Give the extent of all Plasmodium falciparum-infected red blood cells.
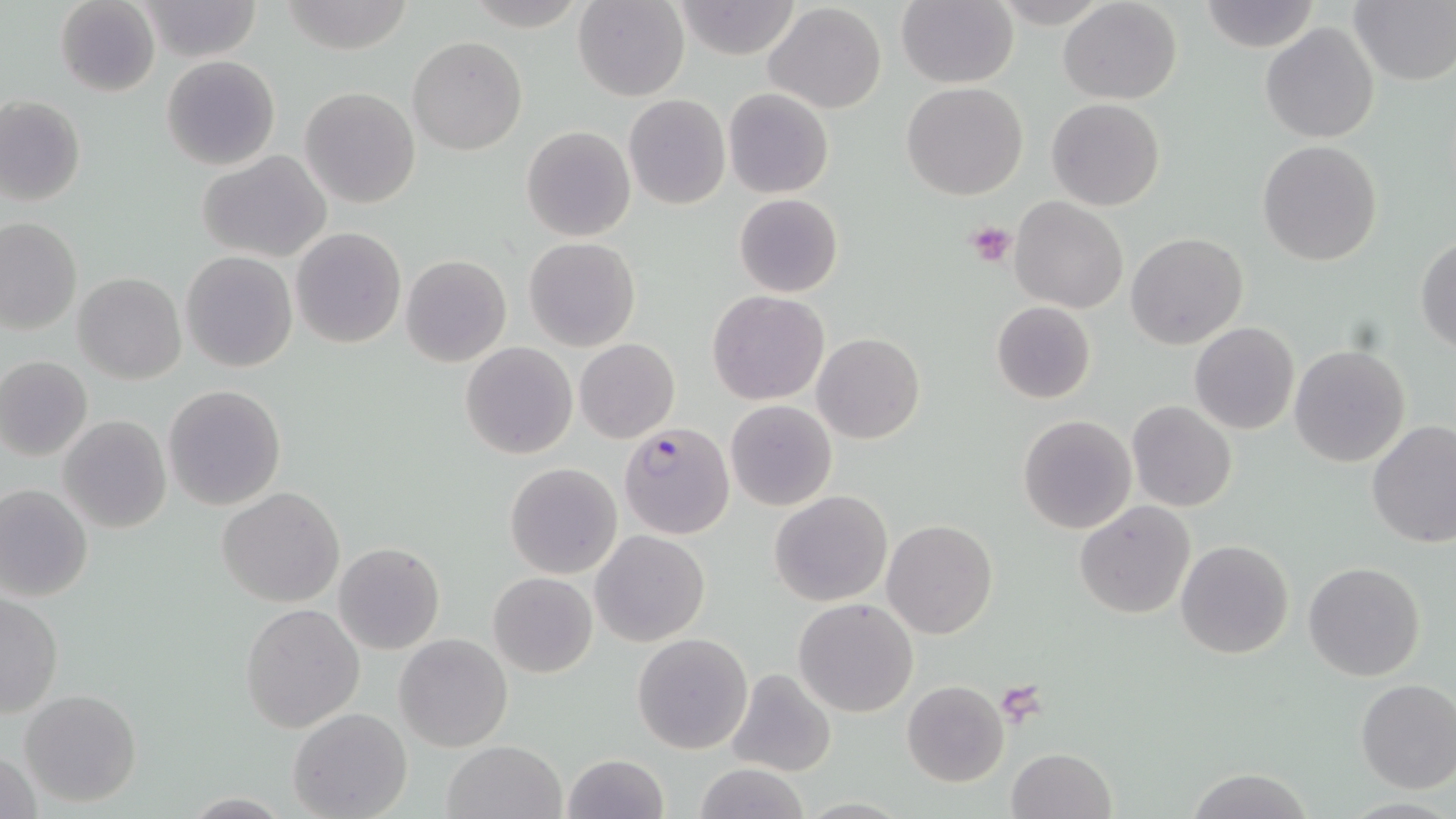

Approximate bounding boxes as (x1,y1)-(x2,y2) corner pairs in pixels.
Plasmodium falciparum-infected red blood cells: (618,421)-(732,540).

Platelet locations: (965,220)-(1018,267), (996,681)-(1048,721). Uninfected red blood cell locations: (137,0)-(264,61), (573,0)-(688,101), (897,0)-(1018,88), (1058,0)-(1184,105), (1198,0)-(1319,52), (56,1)-(160,97), (672,1)-(804,61), (1350,2)-(1455,85), (762,3)-(887,114), (1260,23)-(1380,145), (408,36)-(527,155), (161,55)-(281,171), (902,82)-(1030,201), (299,86)-(420,209), (723,88)-(834,198), (623,95)-(730,209), (0,96)-(86,206), (1046,97)-(1165,211), (520,126)-(636,242), (1257,141)-(1383,266), (197,150)-(332,261), (734,193)-(843,297), (1010,198)-(1128,314), (1,218)-(81,334), (290,227)-(407,348), (1126,233)-(1249,350), (1416,235)-(1456,353), (525,237)-(641,353), (180,251)-(298,372), (400,255)-(512,368), (74,273)-(186,386), (707,290)-(830,406), (991,300)-(1096,404), (1190,323)-(1299,435), (812,332)-(925,443), (574,338)-(679,442), (461,341)-(578,459), (1289,345)-(1411,469), (0,356)-(93,461), (163,384)-(287,511), (724,399)-(838,511), (1126,400)-(1238,512), (1017,414)-(1138,534), (59,415)-(172,533), (1366,422)-(1456,552), (505,462)-(622,578), (0,483)-(94,603), (217,486)-(346,607), (768,489)-(893,606), (1074,500)-(1196,620), (882,519)-(999,639), (590,529)-(711,647), (1174,538)-(1294,659), (335,542)-(444,654), (1303,562)-(1427,682), (488,572)-(597,677), (0,591)-(63,718), (794,598)-(920,718), (240,603)-(365,732), (631,632)-(753,755), (395,634)-(513,752), (726,667)-(836,778), (1354,679)-(1456,794), (901,680)-(1010,787), (19,689)-(142,808), (287,708)-(412,819), (441,740)-(567,819), (1,747)-(44,819), (1006,747)-(1117,819), (561,753)-(668,819), (692,763)-(810,819), (1184,769)-(1312,819). Slide-level diagnosis: Plasmodium falciparum. Optical microscopy. Single field of view. May-Grünwald-Giemsa stain. Image is 1456×819 pixels. 1000x magnification. Thin blood film.